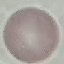

result = no malaria parasites detected
capture = smartphone through the microscope eyepiece
image type = cell patch, automatically extracted from a larger field of view and resized to 64 × 64 pixels
preparation = thin blood smear
stain = Giemsa